Identify the parasite.
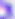
This is Toxoplasma gondii.

Summary:
  - Magnification: 400x
  - Modality: photomicrograph